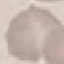

Result: negative for malaria parasites. Giemsa stain. Cell patch, automatically extracted from a larger field of view and resized to 64 × 64 pixels. Thin blood smear. Photographed with a smartphone camera at the microscope eyepiece.